Report the malaria status of this cell.
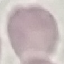

It is uninfected.

Giemsa-stained preparation. Photographed with a smartphone camera at the microscope eyepiece. Cell patch, automatically extracted from a larger field of view and resized to 64 × 64 pixels. Thin smear of blood.